Assess this cell for malaria.
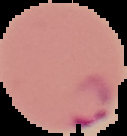
It is parasitized.

preparation = thin blood smear
image size = 127×136 pixels
image type = segmented cell region with the area outside set to black